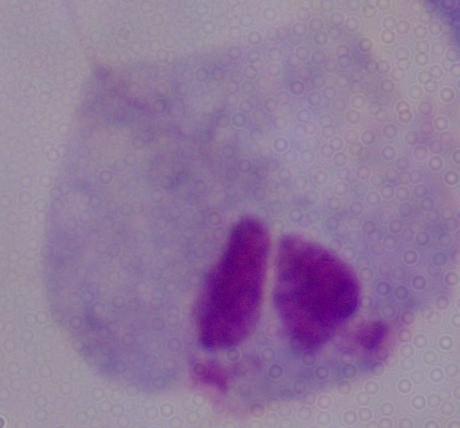
A trichomonad is shown. Micrograph. Captured at 1000x magnification.